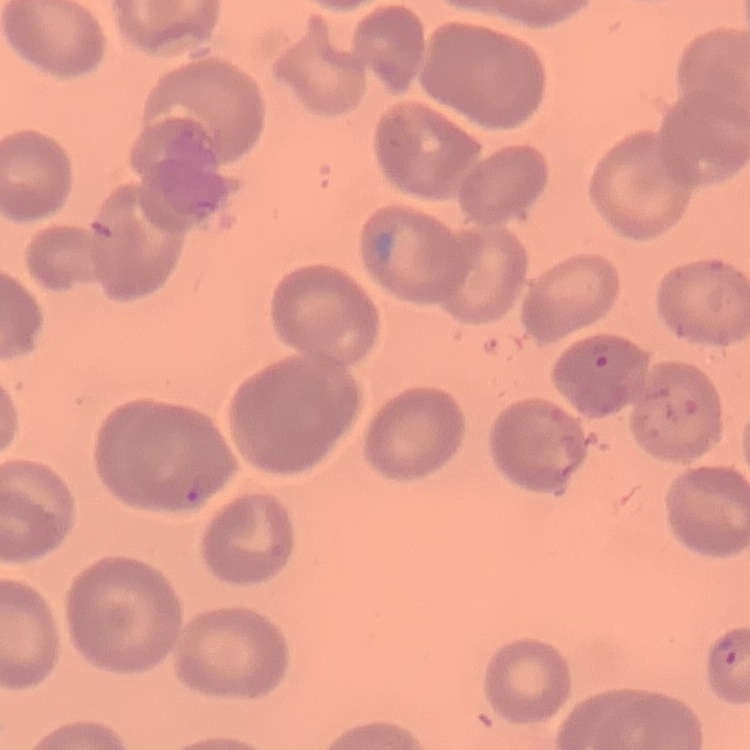

The erythrocytes exhibit no rouleaux formation. One tile cut from a larger photomicrograph. Field's or Giemsa stain. Thin blood smear.